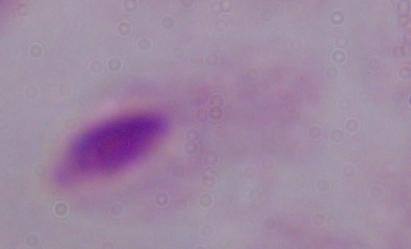 A trichomonad is seen. 1000x magnification. Micrograph.